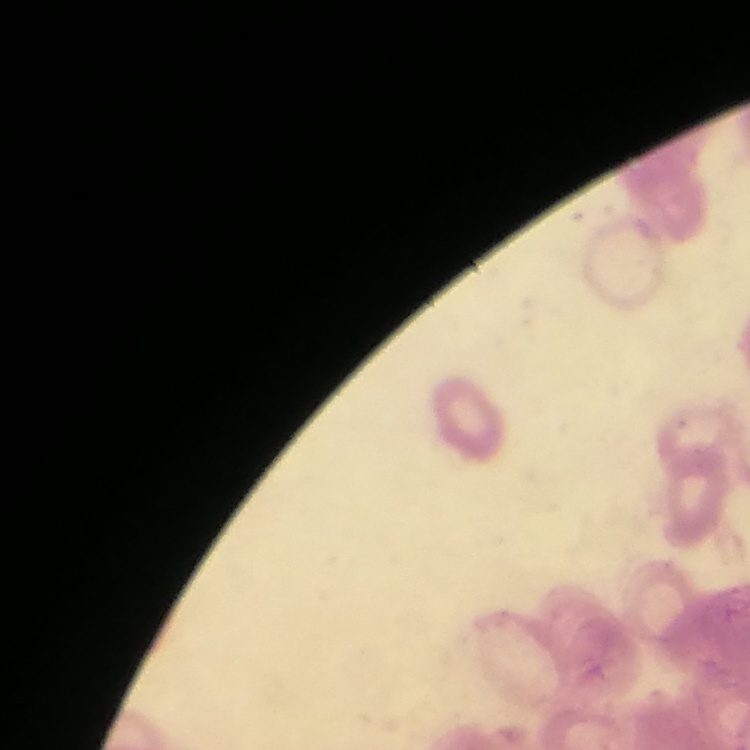 The red blood cells exhibit rouleaux formation. One tile cut from a larger photomicrograph. Thin blood smear. Stained with either Field's or Giemsa.